Comment on the morphology of the red blood cells.
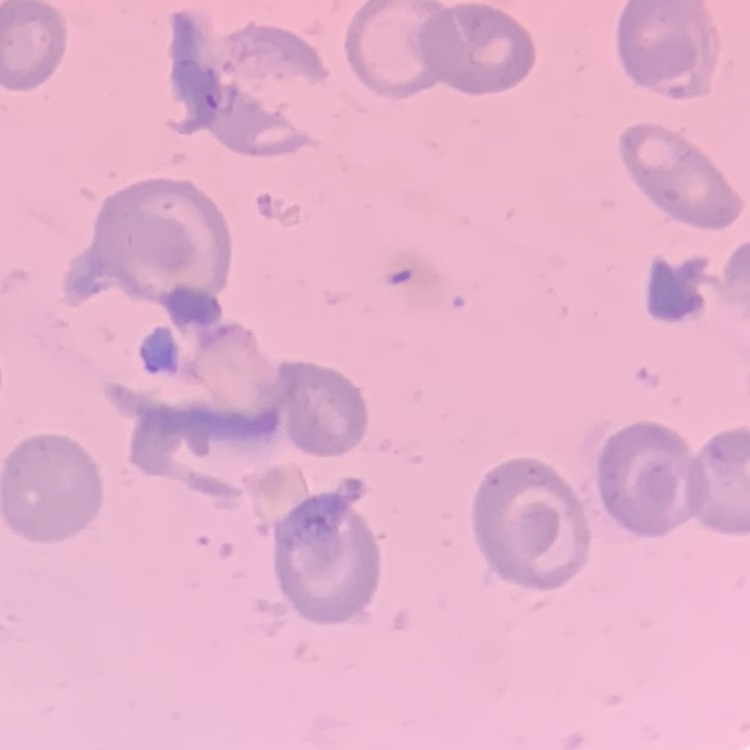

No rouleaux formation.

Field's or Giemsa stain. Square crop of a larger photomicrograph. Thin blood smear.